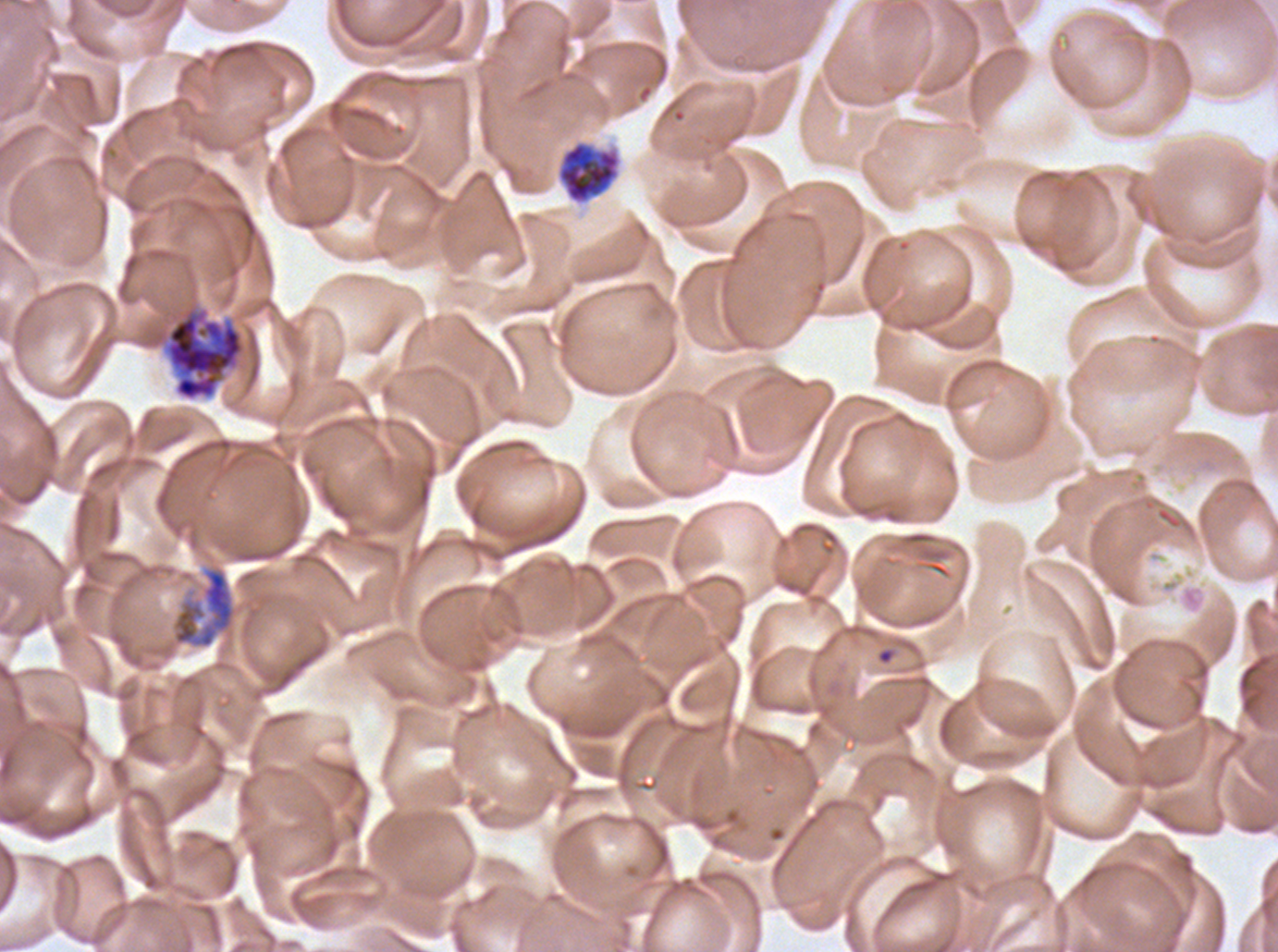
Approximate bounding rectangles given as corner coordinates in pixels from the top-left.
Summary:
  - Early schizont locations: (x1=555, y1=139, x2=622, y2=206), (x1=166, y1=310, x2=244, y2=400), (x1=171, y1=566, x2=237, y2=649)
  - Field of view: one sub-image of a larger composite
  - Stain: Giemsa
  - Preparation: thin blood film
  - Specimen: P. falciparum from a patient in The Gambia, cultured ex vivo for 24 to 48 hours
  - Image size: 1278×952 pixels